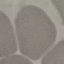
Summary:
  - Malaria status: uninfected
  - Preparation: thin blood film
  - Capture: smartphone camera at the microscope eyepiece
  - Image type: automatically extracted cell patch, resized to 64 × 64 pixels
  - Stain: Giemsa